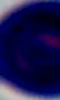

Summary:
  - Modality: micrograph
  - Magnification: 1000x
  - Identification: white blood cell